Point out each Plasmodium parasite.
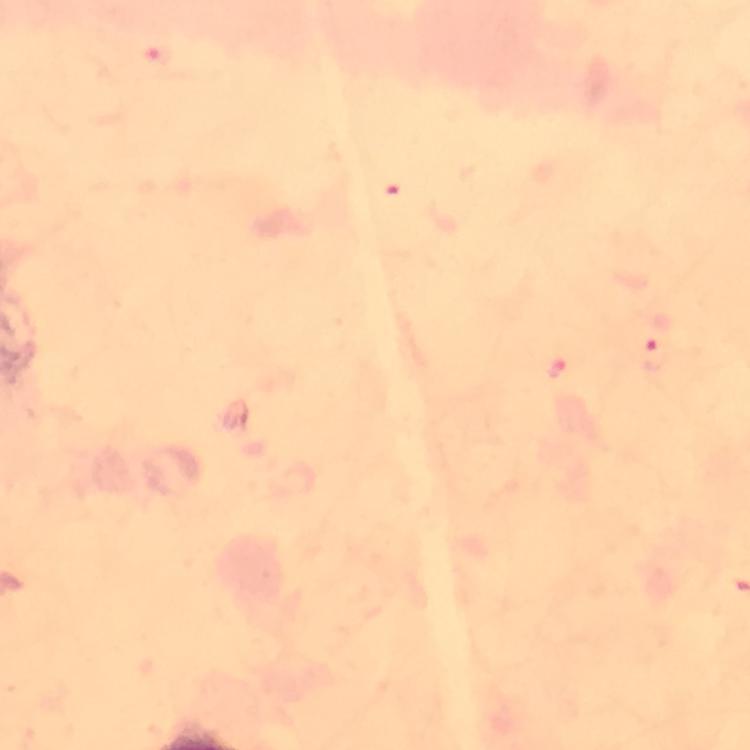
Approximate object centers, in pixels from the top-left corner.
Plasmodium parasites: (x=657, y=345).

Summary:
  - Image size: 750×750 pixels
  - Preparation: thick blood smear
  - Context: from a diagnostic examination for malaria
  - Stain: Giemsa
  - Cropped from: one field of view
  - Capture: smartphone mounted on the microscope
  - Immersion oil: applied
  - Magnification: 100x